Identify the blood parasite species.
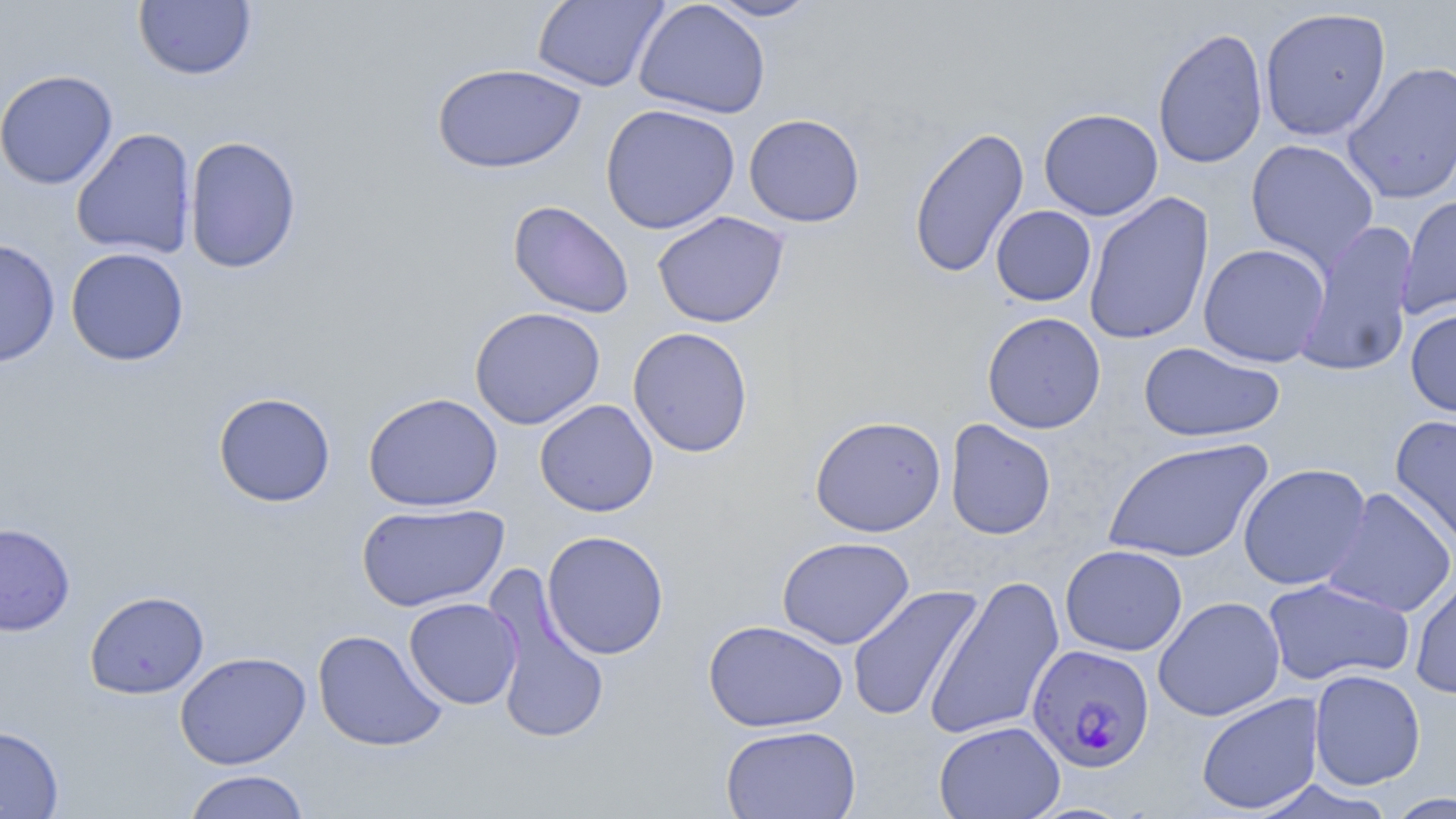

Plasmodium falciparum.

Approximate bounding boxes as [x1, y1, x2, y2] in pixels. Uninfected red blood cell locations: [531, 0, 669, 92], [634, 0, 771, 119], [704, 0, 822, 21], [133, 1, 257, 81], [1259, 6, 1392, 141], [1152, 26, 1268, 170], [1341, 60, 1456, 205], [431, 63, 586, 174], [0, 69, 118, 189], [601, 103, 740, 235], [1038, 107, 1163, 221], [743, 113, 865, 228], [908, 126, 1030, 279], [71, 127, 197, 260], [184, 136, 302, 273], [1245, 139, 1380, 272], [1084, 191, 1215, 346], [1397, 194, 1456, 320], [508, 200, 634, 319], [991, 205, 1096, 306], [651, 211, 789, 329], [1294, 220, 1420, 379], [1, 238, 60, 368], [1198, 243, 1331, 367], [65, 247, 189, 366], [469, 306, 605, 430], [1405, 307, 1456, 417], [982, 312, 1106, 434], [628, 327, 753, 457], [1138, 341, 1285, 443], [213, 392, 336, 507], [363, 393, 503, 512], [534, 399, 659, 517], [809, 414, 946, 537], [1389, 414, 1456, 553], [945, 419, 1056, 540], [1102, 437, 1273, 564], [1237, 463, 1372, 590], [1322, 487, 1456, 618], [357, 502, 509, 612], [0, 522, 75, 636], [541, 530, 669, 659], [777, 536, 914, 649], [1060, 544, 1188, 656], [484, 568, 611, 746], [924, 574, 1065, 742], [1410, 574, 1456, 699], [1261, 577, 1415, 687], [846, 584, 984, 724], [84, 590, 209, 699], [1153, 596, 1285, 722], [404, 597, 522, 709], [703, 619, 848, 733], [312, 629, 448, 752], [174, 651, 311, 769], [1308, 669, 1426, 790], [1196, 693, 1324, 815], [933, 720, 1066, 819], [0, 724, 65, 818], [720, 724, 862, 819], [182, 769, 311, 819], [1384, 792, 1455, 819]. Plasmodium falciparum-infected red blood cell locations: [1026, 643, 1155, 773]. Image is 1456×819 pixels. 1000x magnification. Thin blood smear. One field of a larger specimen. Optical microscopy. May-Grünwald-Giemsa-stained preparation.